Assess this cell for malaria.
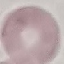
Uninfected.

Thin blood film. Giemsa stain. Automatically extracted cell patch, resized to 64 × 64 pixels. Photographed with a smartphone camera at the microscope eyepiece.